Classify this cell by malaria status.
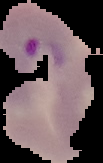
It is parasitized.

Summary:
  - Image type: segmented cell region on a black background
  - Image size: 103×163 pixels
  - Preparation: thin blood smear